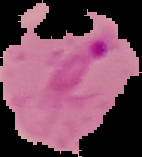
Image is 142×157 pixels. Malaria status: parasitized. From a thin blood film. Cell region segmented out of the field of view; the surrounding area is masked to black.